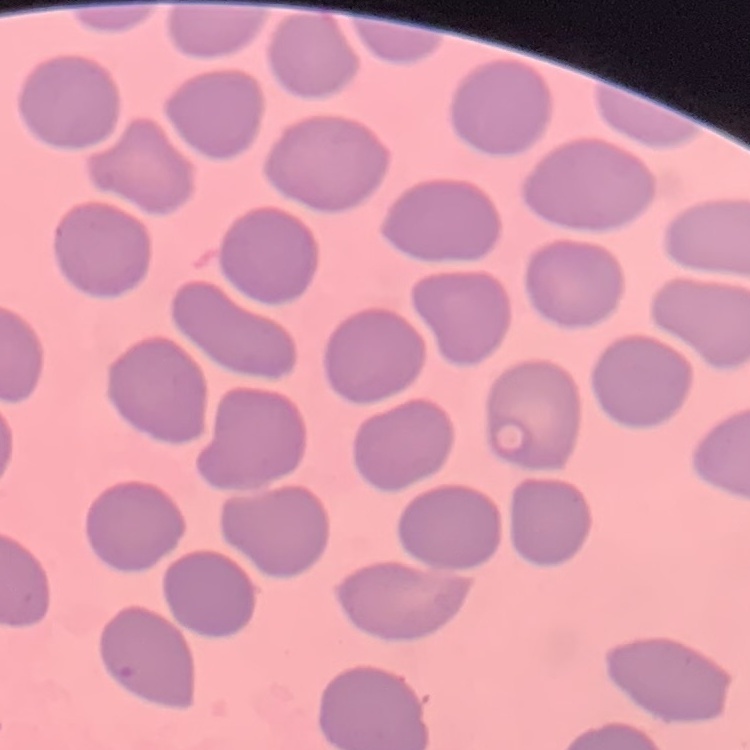
Summary:
  - Erythrocyte morphology: no rouleaux formation
  - Image type: square crop of a larger photomicrograph
  - Stain: Field's or Giemsa
  - Preparation: thin blood film